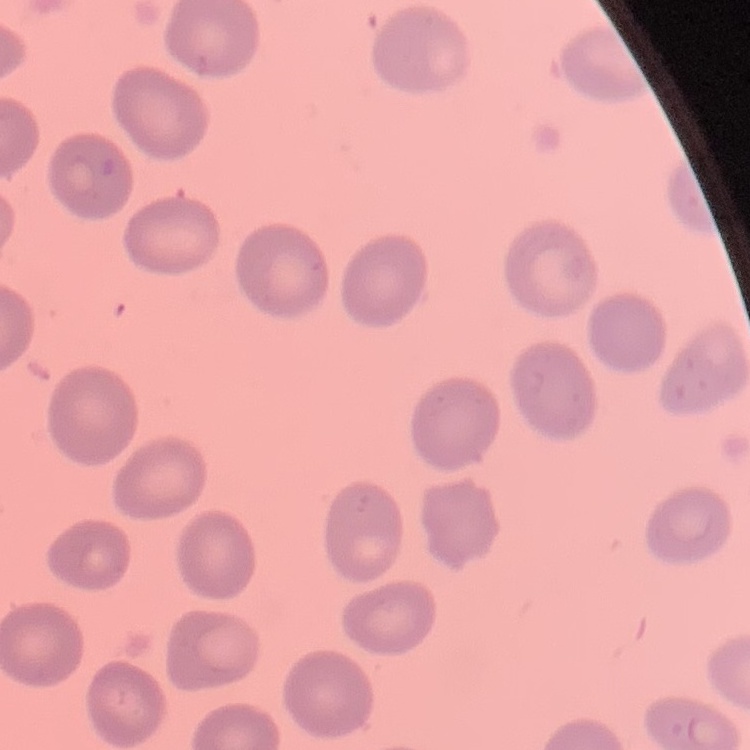

The red blood cells exhibit no rouleaux formation. Stained with either Field's or Giemsa. One tile cut from a larger photomicrograph. Thin blood film.